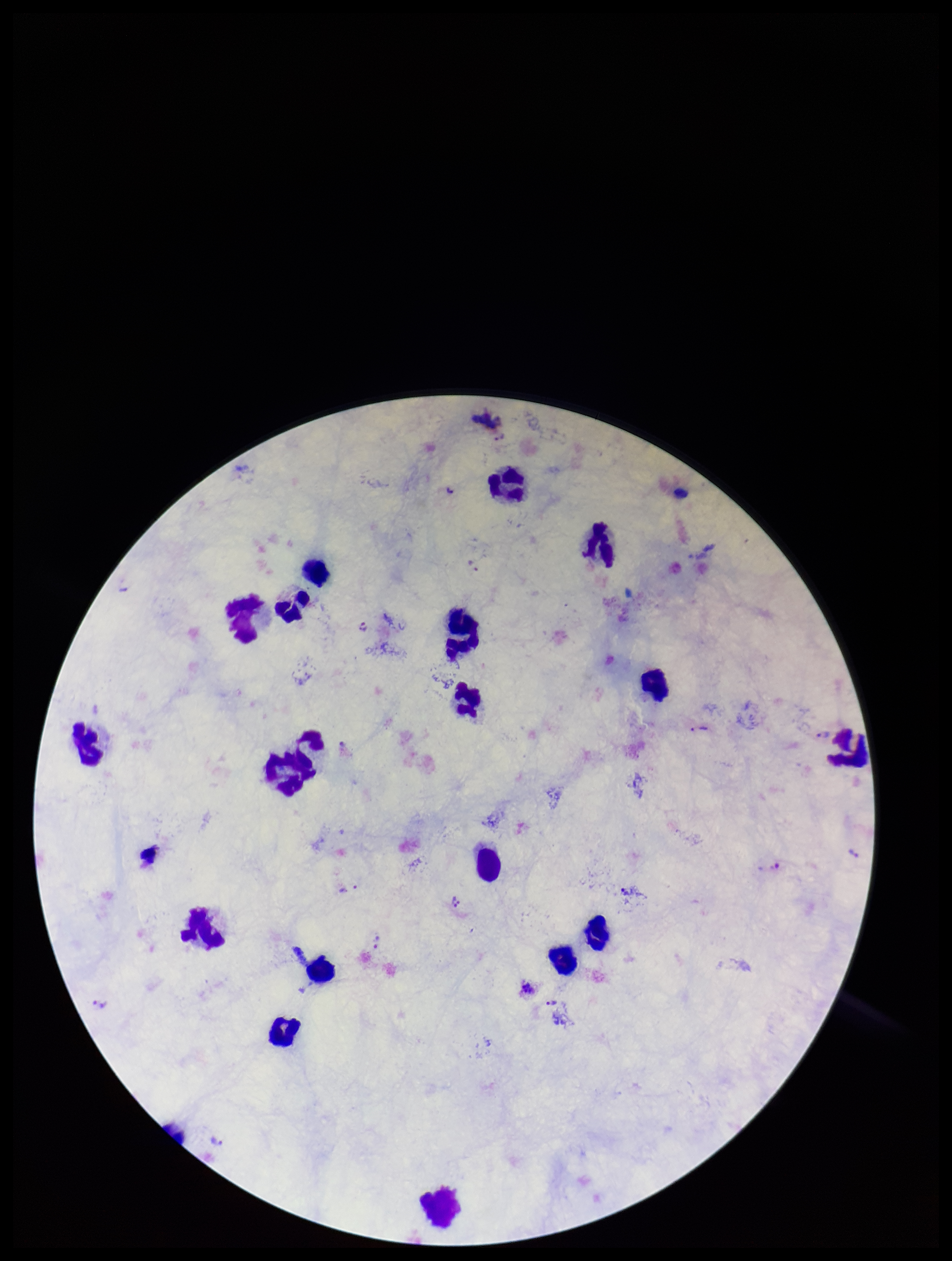

Summary:
  - Stain: Giemsa
  - Capture: smartphone photograph through the microscope eyepiece
  - Parasite count: 12
  - Field of view: one from this slide
  - Plasmodium parasites: seen
  - Preparation: thick
  - Image size: 952×1261 pixels
  - Leukocyte count: 18
  - Patient malaria status: infected
  - Species reported for this patient: Plasmodium vivax